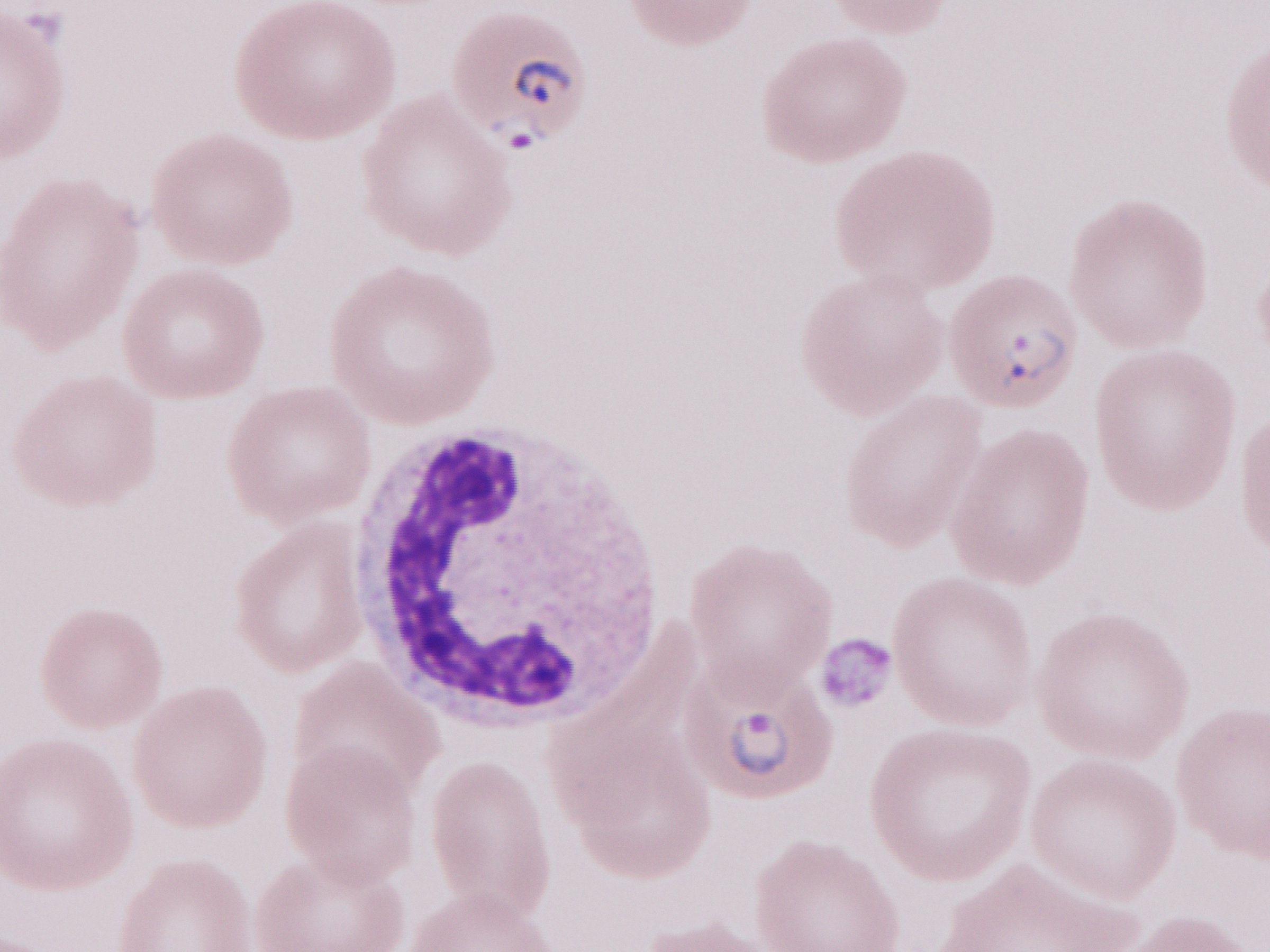 1,000x magnification. Image is 1270×952 pixels. May-Grünwald-Giemsa (MGG) stain. Patient diagnosis: malaria infection. One field of this slide. Thin blood film. Olympus BX43 microscope, Olympus DP73 camera.